Look for Plasmodium parasites.
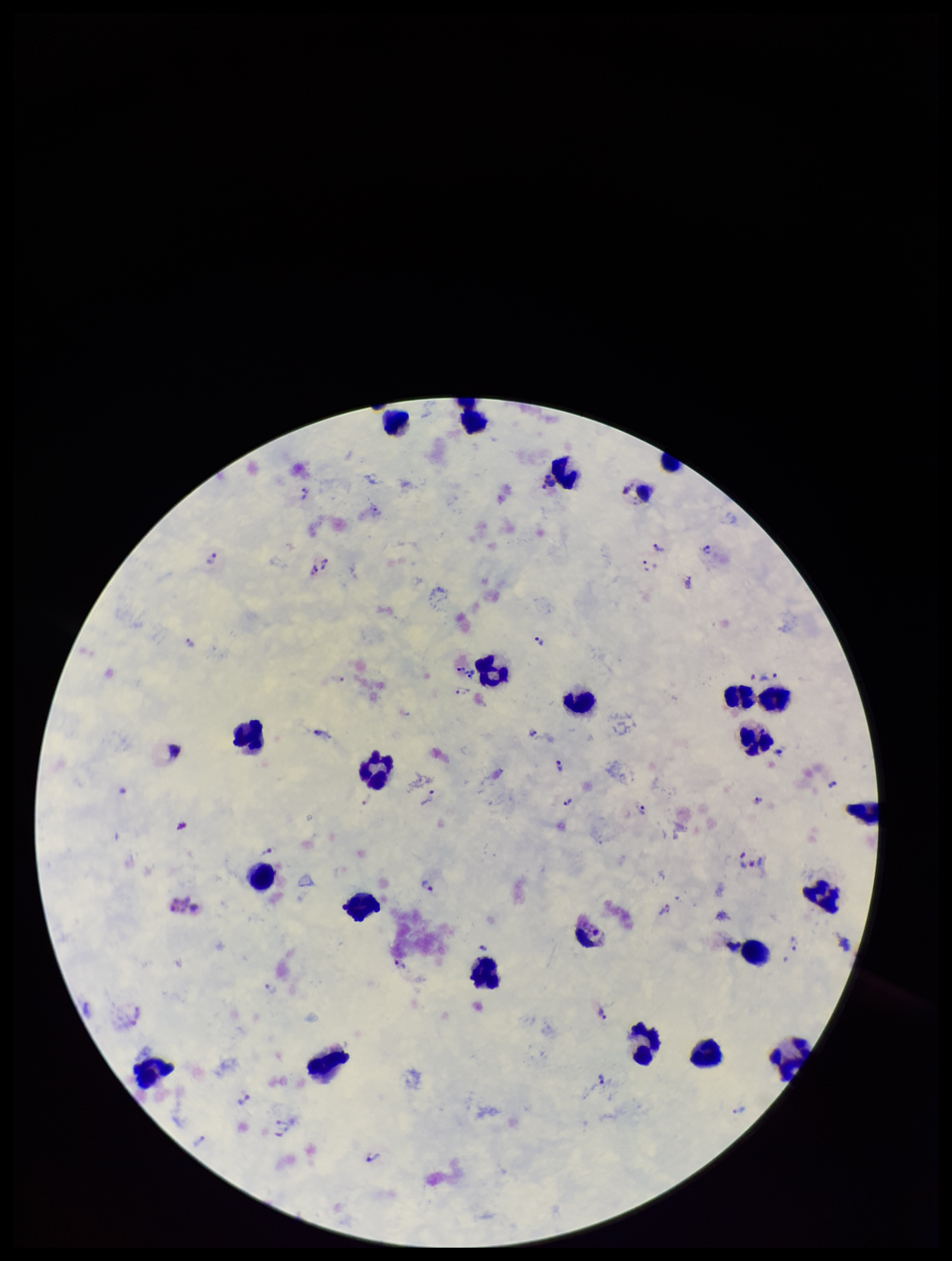
Identified.

Parasite count: 21. Patient malaria status: infected. Smartphone photograph taken through the eyepiece of a microscope. Giemsa stain. Leukocyte count: 24. Image is 952×1261 pixels. Preparation: thick. Single field of view. Species reported for this patient: Plasmodium vivax.